Assess this cell for malaria.
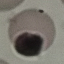
Uninfected.

Cell patch, automatically extracted from a larger field of view and resized to 64 × 64 pixels. Acquired by smartphone through the microscope eyepiece. Thin blood film. Giemsa stain.